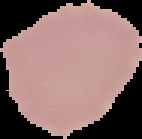

{
  "image_type": "segmented cell region with the area outside set to black",
  "preparation": "thin blood film",
  "result": "no malaria parasites detected",
  "image_size": "142×139 pixels"
}